Assess this cell for malaria.
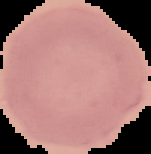
Uninfected.

Summary:
  - Image size: 151×154 pixels
  - Preparation: thin blood film
  - Image type: segmented cell region with the area outside set to black